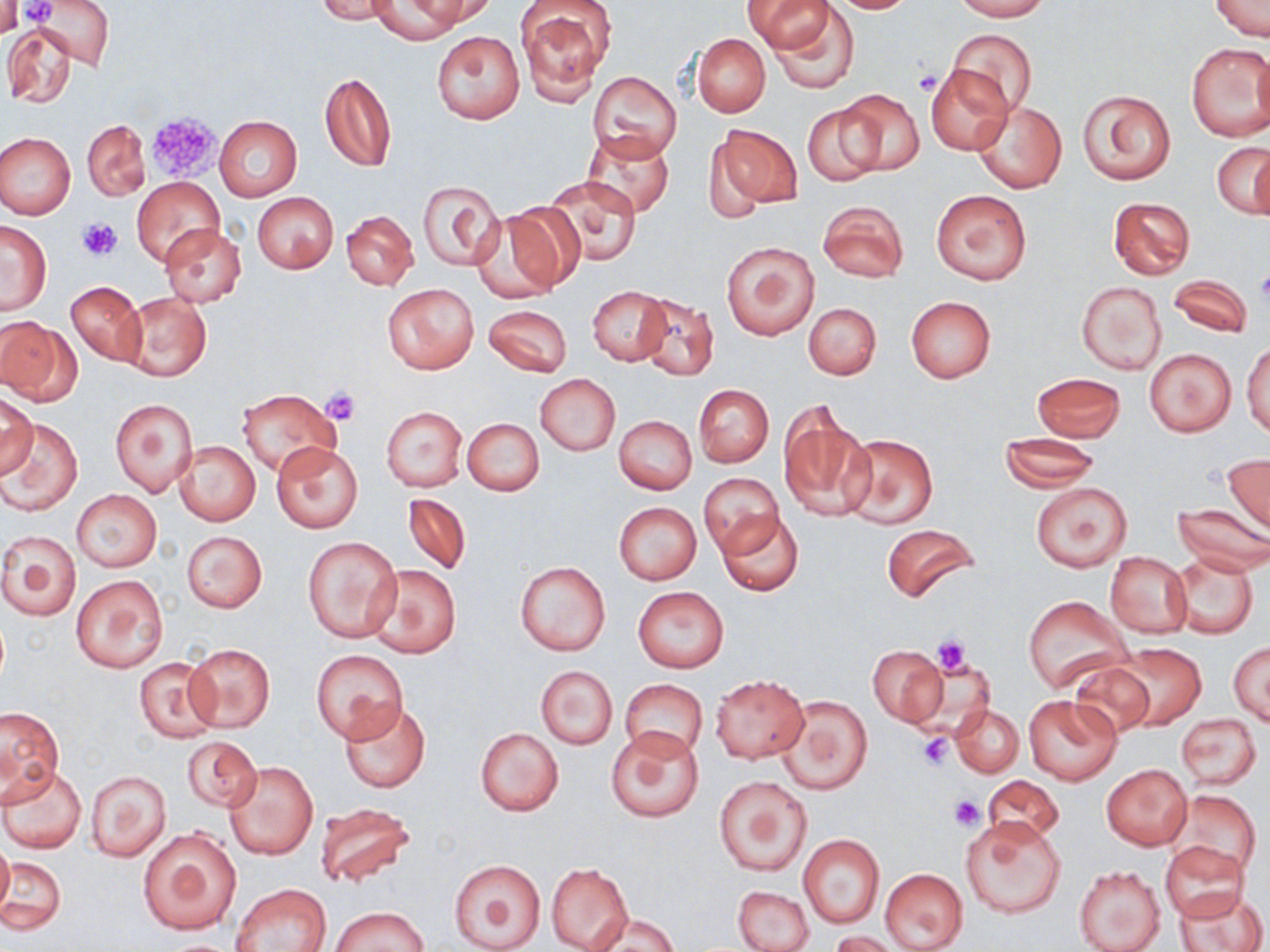
slide-level diagnosis = negative for blood parasites
stain = May-Grünwald-Giemsa
modality = light microscopy
field of view = one of a larger specimen
uninfected red blood cell locations = approximate bounding boxes as (x1,y1)-(x2,y2) corner pairs in pixels: (0,0)-(23,39), (35,0)-(112,67), (318,0)-(397,23), (826,0)-(922,14), (954,0)-(1050,21), (369,1)-(468,42), (413,1)-(495,27), (515,1)-(614,105), (744,1)-(834,53), (1207,1)-(1268,39), (771,4)-(860,96), (3,22)-(77,109), (945,29)-(1038,115), (431,30)-(524,124), (691,34)-(770,117), (1186,42)-(1269,141), (925,66)-(1014,155), (319,70)-(397,173), (590,70)-(682,161), (1078,88)-(1175,185), (839,89)-(924,174), (972,100)-(1066,194), (802,102)-(886,187), (215,116)-(302,200), (82,120)-(150,200), (710,123)-(803,210), (581,131)-(676,217), (0,132)-(76,220), (1213,142)-(1270,217), (542,176)-(643,267), (132,178)-(224,266), (416,179)-(503,270), (931,189)-(1031,286), (252,192)-(339,273), (1107,197)-(1195,280), (818,199)-(908,283), (470,208)-(571,303), (342,211)-(418,290), (1,220)-(52,315), (160,224)-(248,308), (720,240)-(819,340), (1167,274)-(1254,337), (66,280)-(147,366), (1075,280)-(1167,376), (383,283)-(478,374), (587,285)-(671,364), (119,293)-(211,383), (635,293)-(719,381), (905,296)-(996,383), (803,302)-(881,380), (483,304)-(572,377), (0,317)-(80,404), (1243,338)-(1270,437), (1145,348)-(1236,437), (1032,373)-(1126,442), (535,374)-(619,456), (693,384)-(774,468), (236,389)-(339,477), (0,390)-(36,476), (110,398)-(198,497), (777,400)-(875,523), (381,406)-(466,491), (613,415)-(696,494), (0,418)-(83,516), (463,418)-(543,496), (838,433)-(938,530), (1000,433)-(1100,490), (174,440)-(261,526), (272,442)-(362,533), (1223,454)-(1270,535), (699,471)-(783,556), (1031,482)-(1131,571), (70,489)-(162,572), (402,492)-(471,576), (613,503)-(701,584), (1171,503)-(1270,575), (716,509)-(804,598), (880,522)-(981,606), (0,531)-(82,622), (182,531)-(266,612), (304,537)-(401,642), (1104,551)-(1191,638), (1169,551)-(1258,638), (515,561)-(610,656), (364,565)-(460,659), (71,574)-(168,673), (633,587)-(729,673), (1023,595)-(1131,694), (1229,642)-(1269,725), (186,643)-(274,732), (1109,643)-(1205,731), (867,645)-(947,727), (311,651)-(407,743), (134,657)-(219,741), (1069,660)-(1156,738), (534,664)-(617,750), (709,674)-(810,764), (620,679)-(708,761), (773,694)-(873,794), (1023,694)-(1121,785), (339,701)-(430,794), (951,705)-(1024,778), (0,706)-(64,801), (1176,713)-(1261,790), (475,727)-(564,816), (606,728)-(705,823), (183,737)-(261,812), (224,762)-(317,860), (0,765)-(87,854), (1102,765)-(1191,848), (85,768)-(171,862), (981,775)-(1063,846), (714,776)-(813,876), (1166,790)-(1262,877), (316,803)-(416,887), (959,815)-(1065,918), (137,826)-(242,935), (799,834)-(885,930), (1,835)-(14,922), (1159,841)-(1249,921), (0,855)-(65,937), (448,858)-(549,952), (546,863)-(633,951), (1073,865)-(1165,952), (880,868)-(967,952), (232,883)-(331,951), (734,886)-(813,952), (1176,886)-(1266,952), (330,905)-(429,951), (589,911)-(680,952), (831,931)-(899,951)
image size = 1270×952 pixels
platelet locations = approximate bounding boxes as (x1,y1)-(x2,y2) corner pairs in pixels: (15,0)-(58,26), (914,70)-(941,96), (146,112)-(221,181), (77,218)-(121,260), (1254,270)-(1270,304), (320,386)-(361,426), (931,635)-(971,676), (918,734)-(953,768), (949,795)-(985,830)
magnification = 1000x
preparation = thin blood smear